Locate every leukocyte (white blood cell).
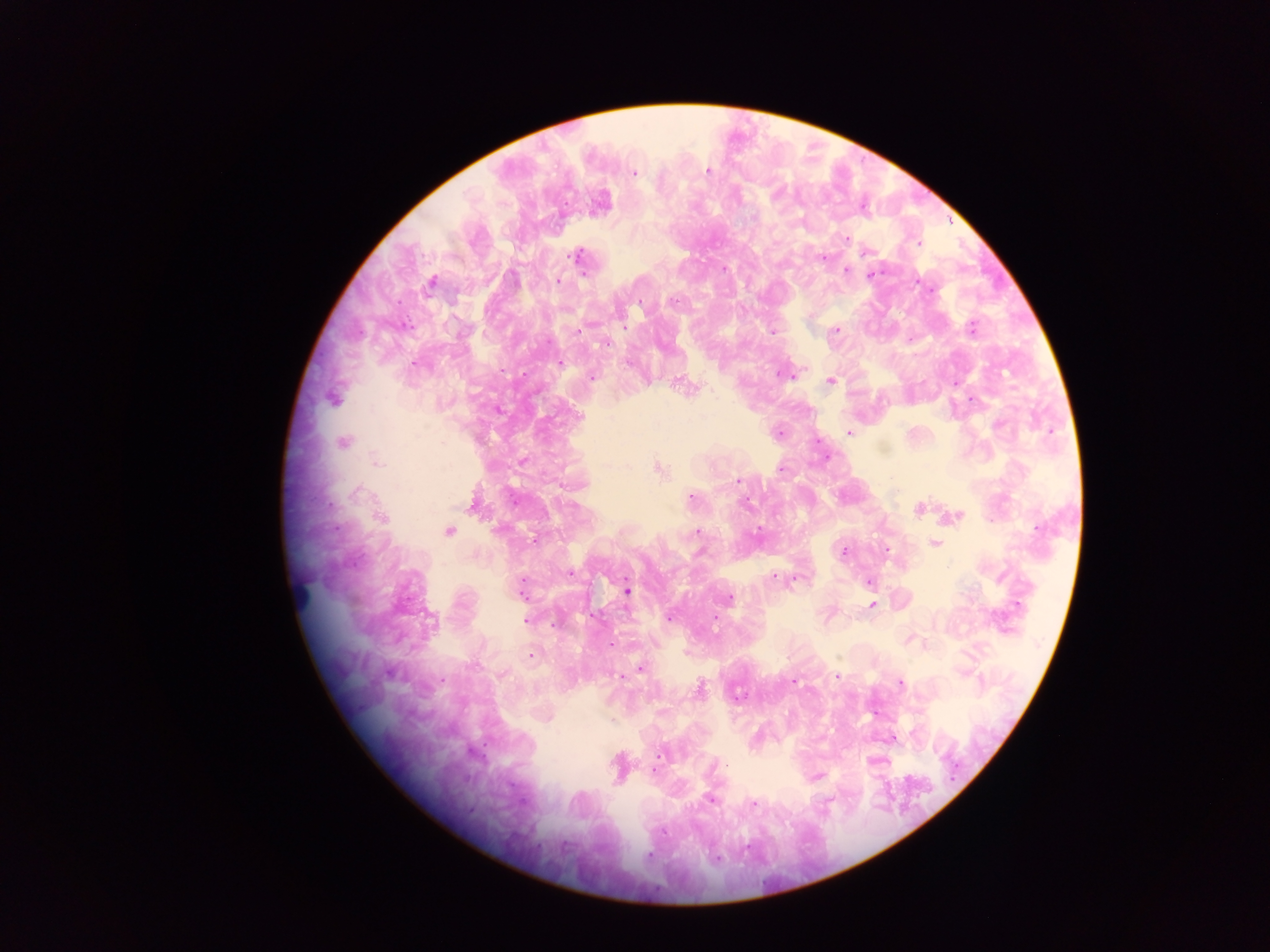
Approximate centers as {x, y} in pixels.
Leukocytes: {298, 593}.

{
  "field_of_view": "single",
  "malaria_parasite_locations": "approximate centers as {x, y} in pixels: {708, 171}, {633, 173}, {847, 238}, {919, 243}, {578, 256}, {822, 257}, {846, 270}, {871, 275}, {557, 281}, {432, 282}, {672, 300}, {971, 328}, {836, 330}, {578, 331}, {772, 332}, {605, 344}, {560, 363}, {782, 374}, {591, 377}, {830, 380}, {332, 399}, {972, 399}, {579, 417}, {848, 433}, {343, 443}, {377, 462}, {658, 468}, {780, 469}, {738, 482}, {357, 492}, {692, 499}, {919, 510}, {955, 516}, {381, 517}, {1037, 528}, {448, 531}, {698, 532}, {534, 539}, {934, 543}, {887, 549}, {844, 551}, {570, 574}, {774, 577}, {868, 582}, {521, 587}, {627, 591}, {729, 597}, {872, 606}, {669, 619}, {525, 621}, {611, 645}, {531, 656}, {640, 669}, {503, 675}, {836, 675}, {621, 677}, {442, 680}, {792, 682}, {900, 684}, {699, 690}, {659, 755}, {654, 771}, {816, 776}, {711, 800}, {753, 803}, {649, 856}",
  "capture": "mobile-phone photograph through a microscope",
  "country": "Ghana",
  "preparation": "thick blood film",
  "image_size": "1270×952 pixels"
}